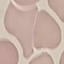
malaria status = uninfected
stain = Giemsa
preparation = thin smear
capture = smartphone camera at the microscope eyepiece
image type = cell patch, automatically extracted from a larger field of view and resized to 64 × 64 pixels